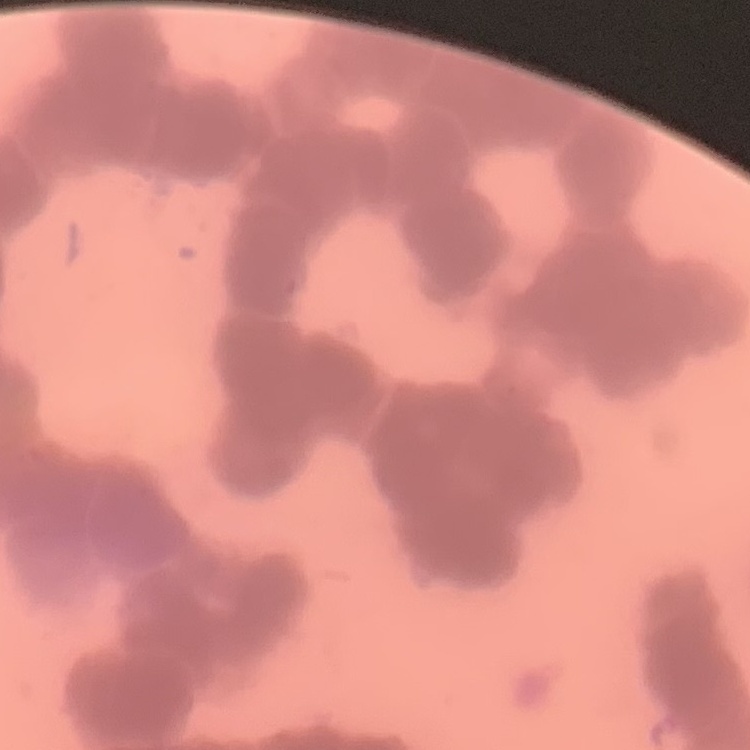

The erythrocytes show rouleaux formation. Square crop of a larger photomicrograph. Thin blood smear. Stained with either Field's or Giemsa.